Report the malaria status of this cell.
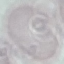

Uninfected.

Summary:
  - Preparation: thin blood film
  - Stain: Giemsa
  - Capture: smartphone camera at the microscope eyepiece
  - Image type: cell patch, automatically extracted from a larger field of view and resized to 64 × 64 pixels